Locate every malaria parasite.
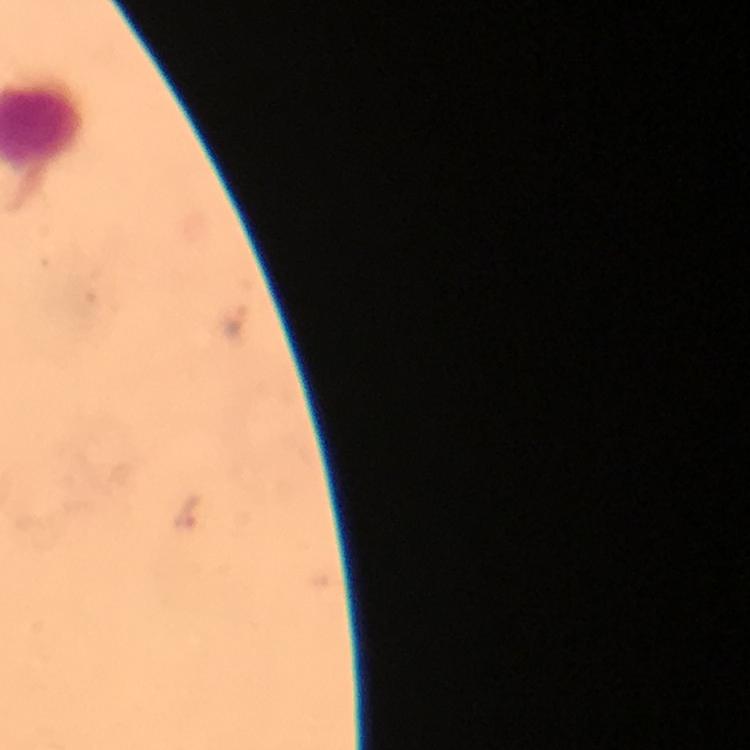

Approximate centers as [x, y] in pixels.
Malaria parasites: [237, 325], [188, 512].

At 100x magnification. A crop from one field of view. Image is 750×750 pixels. Immersion oil was used. Giemsa stain. Smartphone photograph taken through a microscope. From a diagnostic examination for malaria. Thick blood film.